Name the parasite shown.
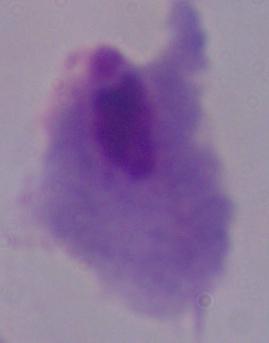
A trichomonad.

Summary:
  - Modality: micrograph
  - Magnification: 1000x